Point out each Plasmodium parasite.
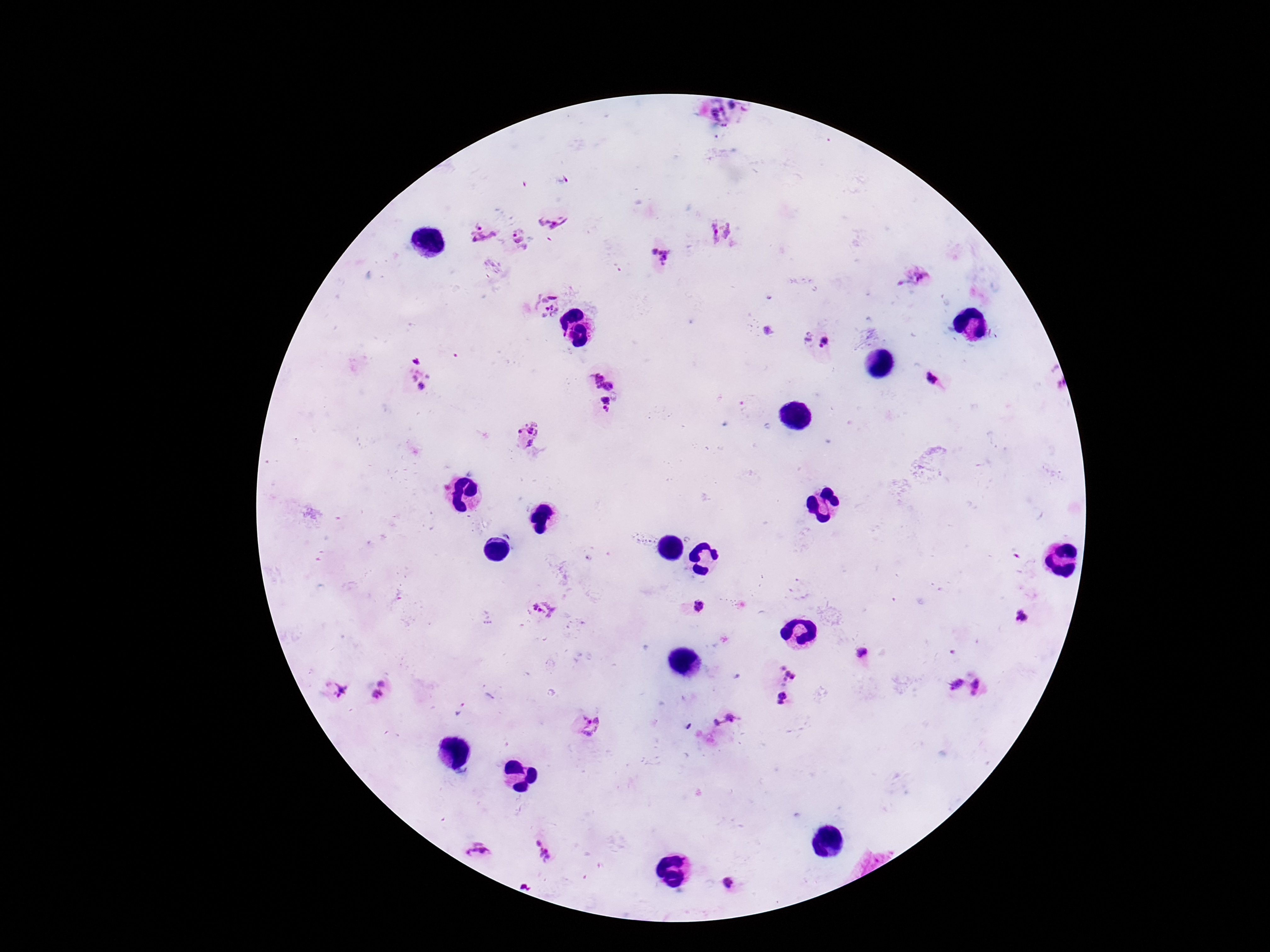

Approximate centers as [x, y] in pixels.
Plasmodium parasites: [732, 106], [715, 112], [723, 125], [718, 137], [563, 180], [550, 221], [721, 232], [483, 233], [520, 241], [661, 256], [493, 267], [922, 277], [546, 304], [808, 336], [824, 341], [417, 359], [603, 378], [421, 379], [932, 379], [605, 402], [526, 435], [700, 606], [546, 609], [1021, 616], [862, 653], [787, 677], [382, 681], [955, 683], [978, 687], [339, 689], [376, 694], [781, 697], [461, 709], [723, 720], [587, 724], [542, 850], [477, 852], [729, 882], [526, 883].

Summary:
  - Patient malaria status: infected
  - Image size: 1270×952 pixels
  - Stain: Giemsa
  - Magnification: 100x
  - Preparation: thick peripheral-blood smear
  - Field of view: single
  - Capture: smartphone camera through the microscope eyepiece